Name the blood parasite species.
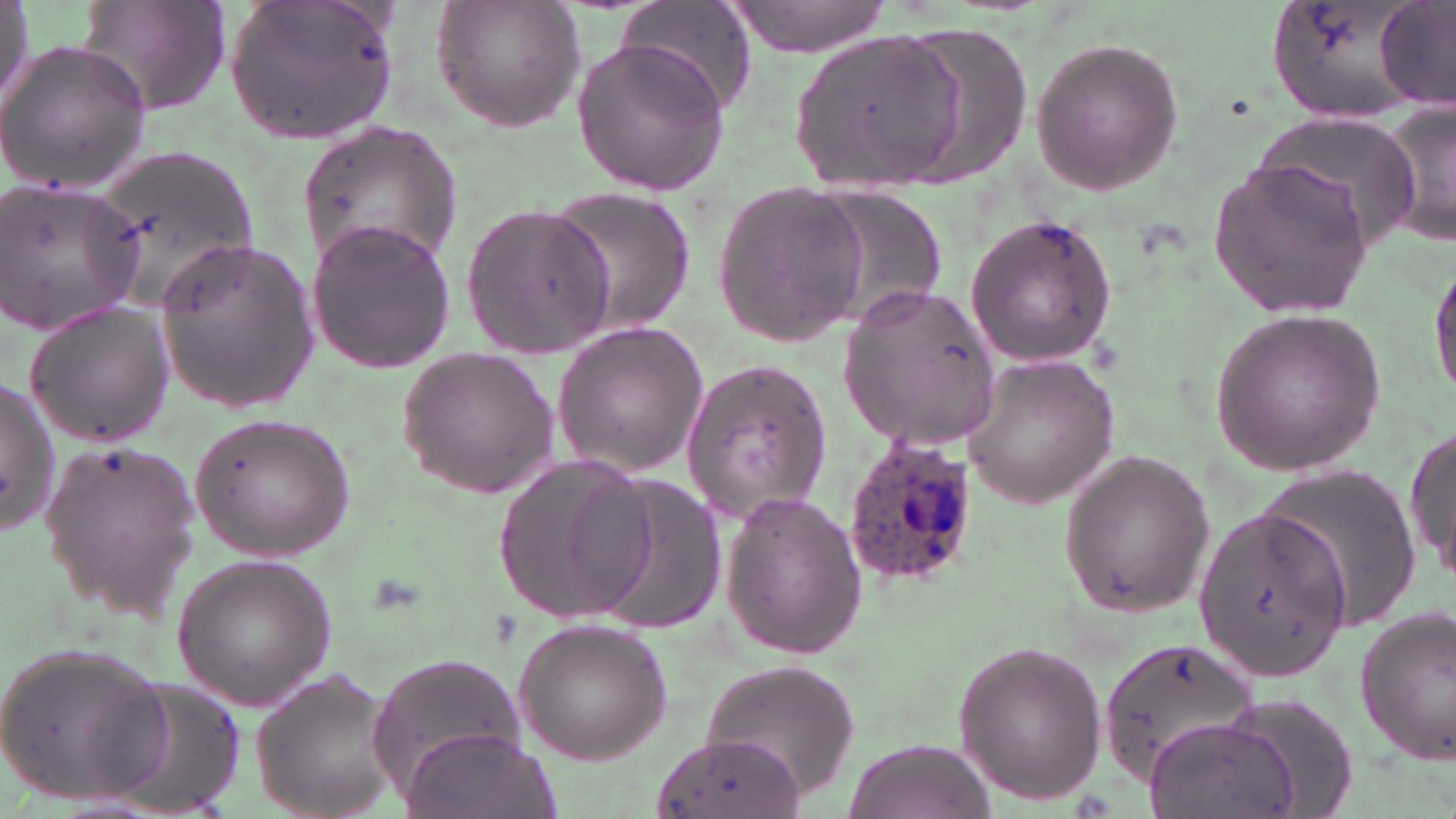

Plasmodium ovale.

Summary:
  - Coordinate format: approximate bounding boxes as named x1/y1/x2/y2 corners in pixels
  - Uninfected red blood cell locations: (x1=0, y1=0, x2=32, y2=110), (x1=78, y1=0, x2=231, y2=115), (x1=225, y1=0, x2=403, y2=142), (x1=431, y1=0, x2=587, y2=133), (x1=619, y1=0, x2=757, y2=117), (x1=723, y1=0, x2=897, y2=59), (x1=1265, y1=0, x2=1425, y2=125), (x1=1375, y1=0, x2=1453, y2=108), (x1=891, y1=25, x2=1032, y2=187), (x1=795, y1=32, x2=974, y2=196), (x1=568, y1=35, x2=732, y2=196), (x1=1026, y1=37, x2=1187, y2=198), (x1=0, y1=38, x2=152, y2=191), (x1=1374, y1=97, x2=1456, y2=254), (x1=1248, y1=113, x2=1416, y2=252), (x1=298, y1=126, x2=462, y2=275), (x1=91, y1=140, x2=264, y2=307), (x1=1207, y1=157, x2=1374, y2=319), (x1=0, y1=178, x2=145, y2=334), (x1=710, y1=182, x2=865, y2=349), (x1=805, y1=185, x2=950, y2=327), (x1=538, y1=186, x2=698, y2=336), (x1=461, y1=202, x2=616, y2=359), (x1=962, y1=213, x2=1120, y2=367), (x1=307, y1=218, x2=457, y2=372), (x1=155, y1=236, x2=316, y2=412), (x1=1429, y1=252, x2=1456, y2=406), (x1=838, y1=283, x2=1002, y2=449), (x1=23, y1=300, x2=173, y2=449), (x1=1209, y1=306, x2=1391, y2=478), (x1=550, y1=319, x2=709, y2=476), (x1=396, y1=344, x2=560, y2=500), (x1=961, y1=351, x2=1120, y2=504), (x1=678, y1=360, x2=831, y2=521), (x1=0, y1=379, x2=60, y2=534), (x1=188, y1=412, x2=354, y2=562), (x1=1406, y1=413, x2=1454, y2=585), (x1=37, y1=439, x2=206, y2=616), (x1=1058, y1=448, x2=1217, y2=618), (x1=493, y1=455, x2=656, y2=626), (x1=1251, y1=465, x2=1421, y2=632), (x1=591, y1=475, x2=731, y2=635), (x1=717, y1=494, x2=868, y2=658), (x1=1194, y1=507, x2=1350, y2=679), (x1=172, y1=550, x2=336, y2=712), (x1=1354, y1=606, x2=1456, y2=767), (x1=514, y1=617, x2=671, y2=765), (x1=1096, y1=637, x2=1257, y2=783), (x1=951, y1=641, x2=1107, y2=805), (x1=0, y1=642, x2=170, y2=809), (x1=370, y1=652, x2=527, y2=792), (x1=697, y1=656, x2=865, y2=801), (x1=249, y1=669, x2=402, y2=819), (x1=98, y1=678, x2=245, y2=817), (x1=1221, y1=691, x2=1361, y2=817), (x1=1143, y1=715, x2=1296, y2=819), (x1=401, y1=727, x2=553, y2=819), (x1=655, y1=730, x2=805, y2=819), (x1=844, y1=734, x2=993, y2=818)
  - Plasmodium ovale-infected red blood cell locations: (x1=836, y1=436, x2=976, y2=588)
  - Modality: optical microscopy
  - Image size: 1456×819 pixels
  - Field of view: one of a larger specimen
  - Magnification: 1000x
  - Preparation: thin blood film
  - Stain: May-Grünwald-Giemsa